Report the malaria status of this cell.
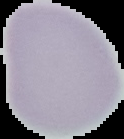

It is uninfected.

Image is 124×139 pixels. From a thin blood smear. Segmented cell region on a black background.